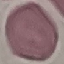
Result: no malaria parasites seen. Giemsa stain. Photographed with a smartphone camera at the microscope eyepiece. Thin smear of blood. Cell patch, automatically extracted from a larger field of view and resized to 64 × 64 pixels.